Name the parasite shown.
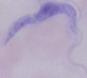

This is a trypanosome.

Summary:
  - Modality: photomicrograph
  - Magnification: 1000x